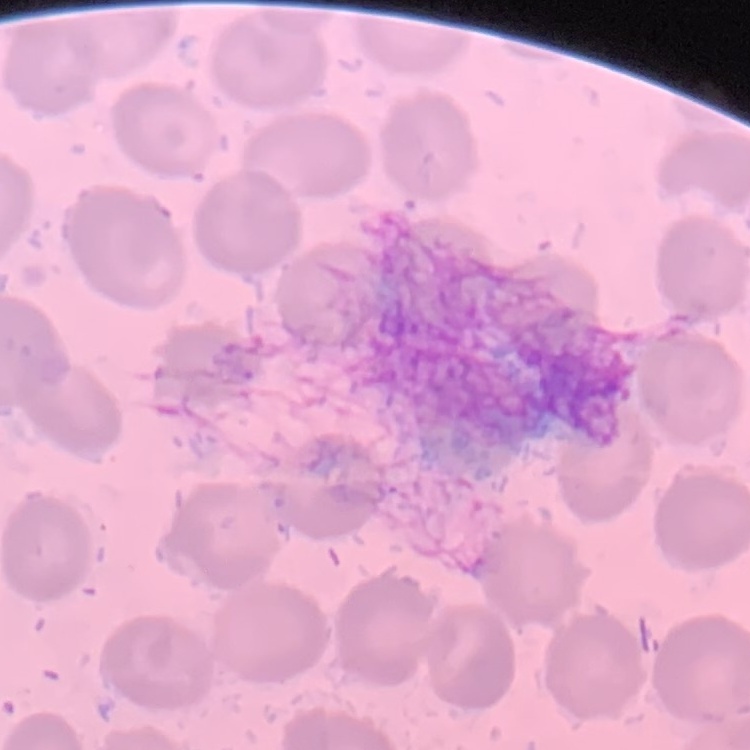

red blood cell morphology = no rouleaux formation
preparation = thin blood film
image type = one tile cut from a larger photomicrograph
stain = Field's or Giemsa